Classify this cell by malaria status.
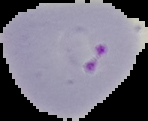

Parasitized.

Image is 148×121 pixels. The area outside the segmented cell region is set to black. From a thin blood smear.